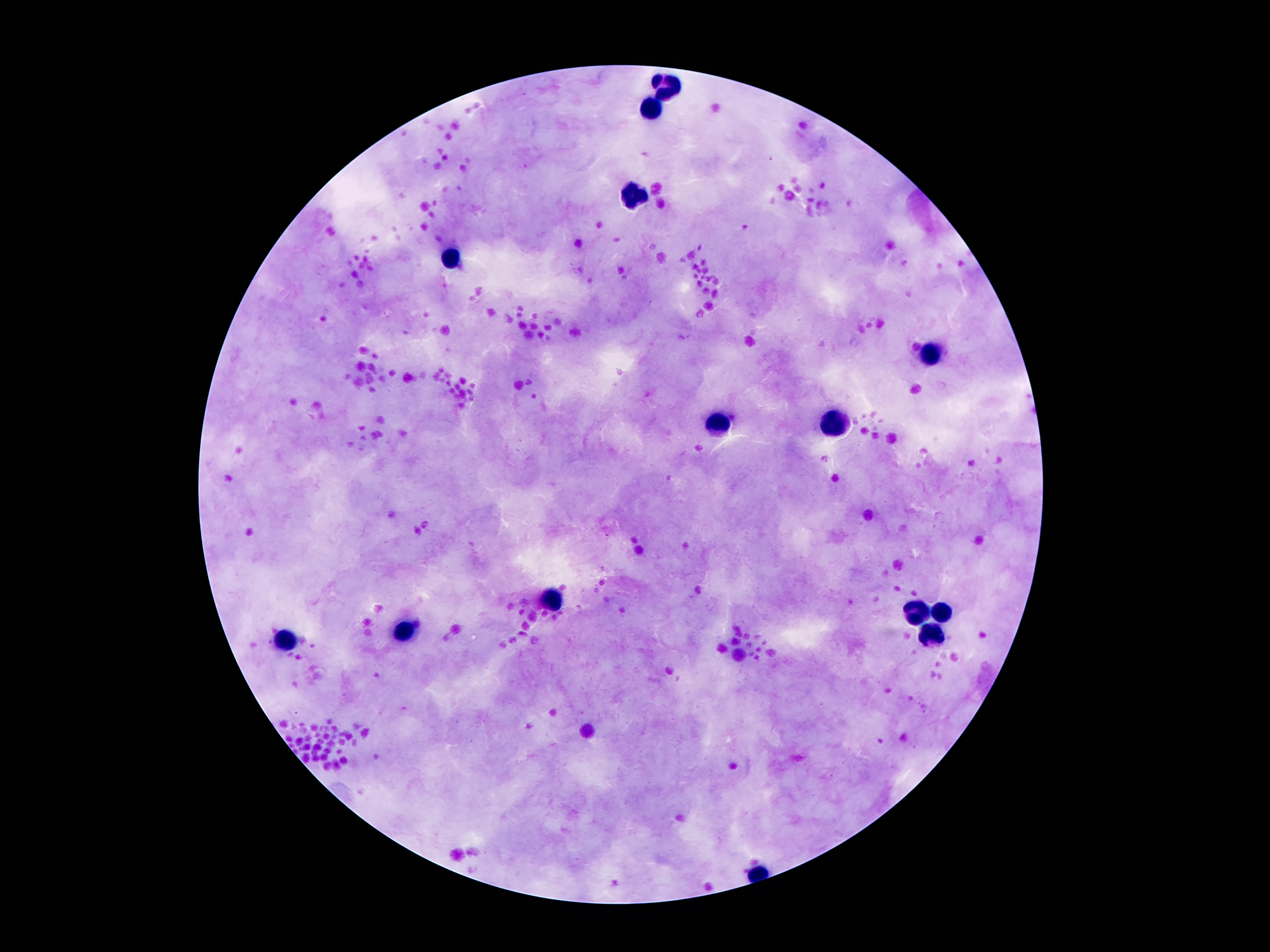

image_size: 1270×952 pixels
leukocyte_locations: 'approximate centers as (x, y) in pixels: (666, 86), (651, 106), (632, 193), (452, 258), (931, 353), (717, 423), (832, 426), (555, 599), (914, 613), (941, 613), (406, 631), (931, 638), (286, 641)'
capture: smartphone camera through the microscope eyepiece
preparation: thick peripheral-blood smear
patient_malaria_status: not infected
magnification: 100x
stain: Giemsa
field_of_view: single